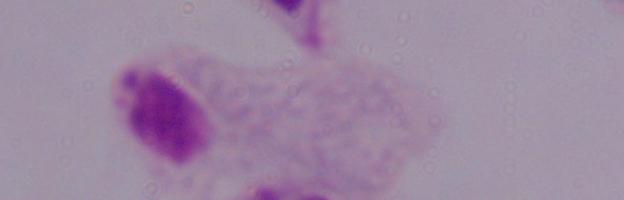

identification: trichomonad
modality: photomicrograph
magnification: 1000x